State which cell type is depicted.
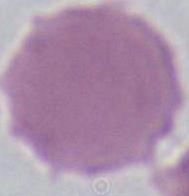

This is an erythrocyte.

1000x magnification. Photomicrograph.